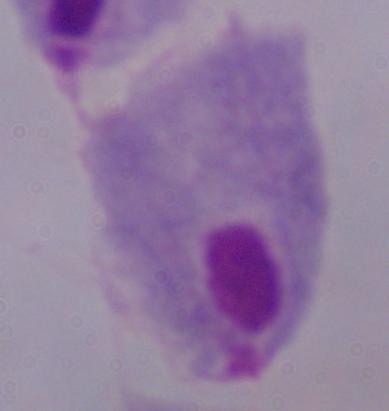
Summary:
  - Modality: micrograph
  - Identification: trichomonad
  - Magnification: 1000x